Describe the morphology of the erythrocytes.
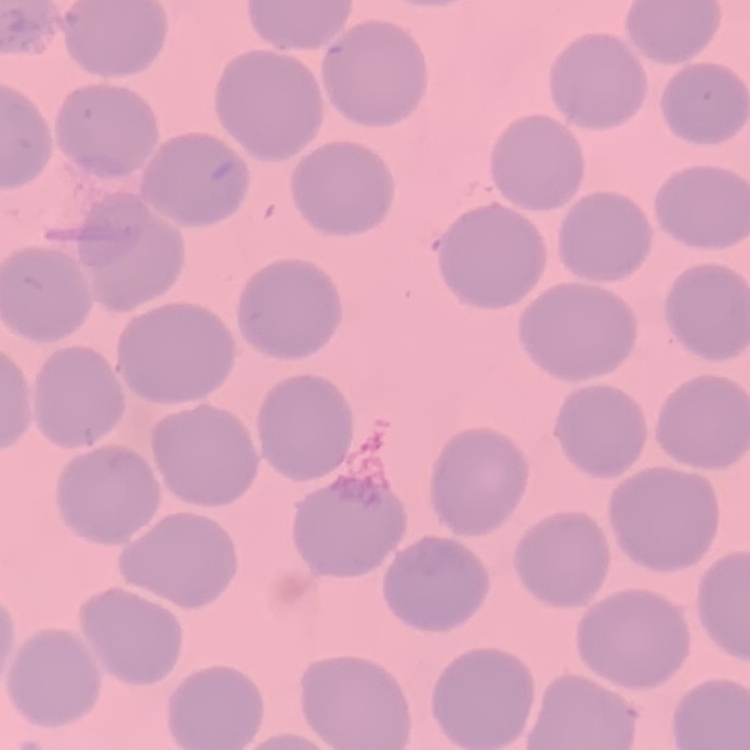

They show no rouleaux formation.

stain = Field's or Giemsa
preparation = thin peripheral smear
image type = square crop of a larger photomicrograph